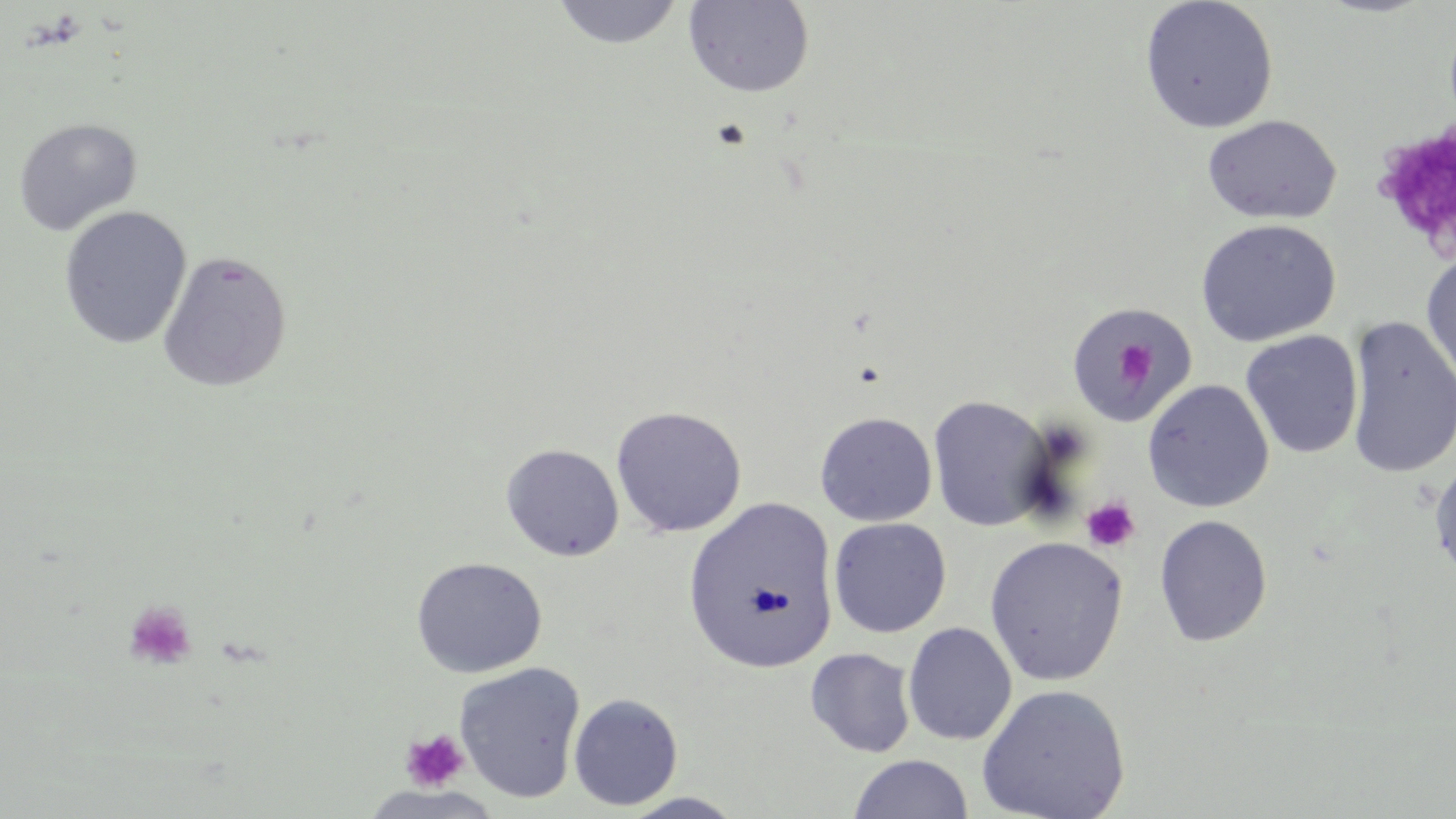
Approximate bounding boxes as [x1, y1, x2, y2] in pixels. Uninfected red blood cell locations: [549, 0, 686, 51], [1139, 0, 1278, 134], [682, 1, 815, 97], [1202, 115, 1341, 224], [13, 117, 142, 235], [58, 206, 192, 349], [1195, 218, 1342, 347], [1421, 249, 1456, 394], [157, 250, 293, 392], [1065, 303, 1195, 421], [1344, 316, 1456, 480], [1240, 330, 1364, 459], [1142, 379, 1274, 513], [927, 395, 1054, 532], [610, 405, 747, 537], [814, 411, 937, 526], [500, 442, 625, 561], [1429, 454, 1456, 583], [682, 498, 840, 673], [1153, 514, 1273, 646], [828, 516, 951, 638], [984, 536, 1129, 687], [410, 556, 547, 678], [902, 622, 1017, 745], [805, 647, 916, 758], [454, 662, 586, 803], [975, 684, 1130, 819], [568, 693, 683, 811], [848, 754, 974, 818], [618, 792, 749, 818]. Platelet locations: [1372, 122, 1456, 257], [1111, 336, 1162, 390], [1080, 496, 1141, 553], [122, 600, 199, 672], [399, 729, 470, 793]. Slide-level diagnosis: negative for blood parasites. Thin blood smear. One field of a larger specimen. May-Grünwald-Giemsa-stained preparation. Optical microscopy. Captured at 1000x magnification. Image is 1456×819 pixels.